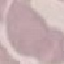 Result: negative for malaria parasites. Acquired by smartphone through the microscope eyepiece. Thin blood smear. Giemsa-stained preparation. Cell patch, automatically extracted from a larger field of view and resized to 64 × 64 pixels.